Locate every blood parasite and identify its species.
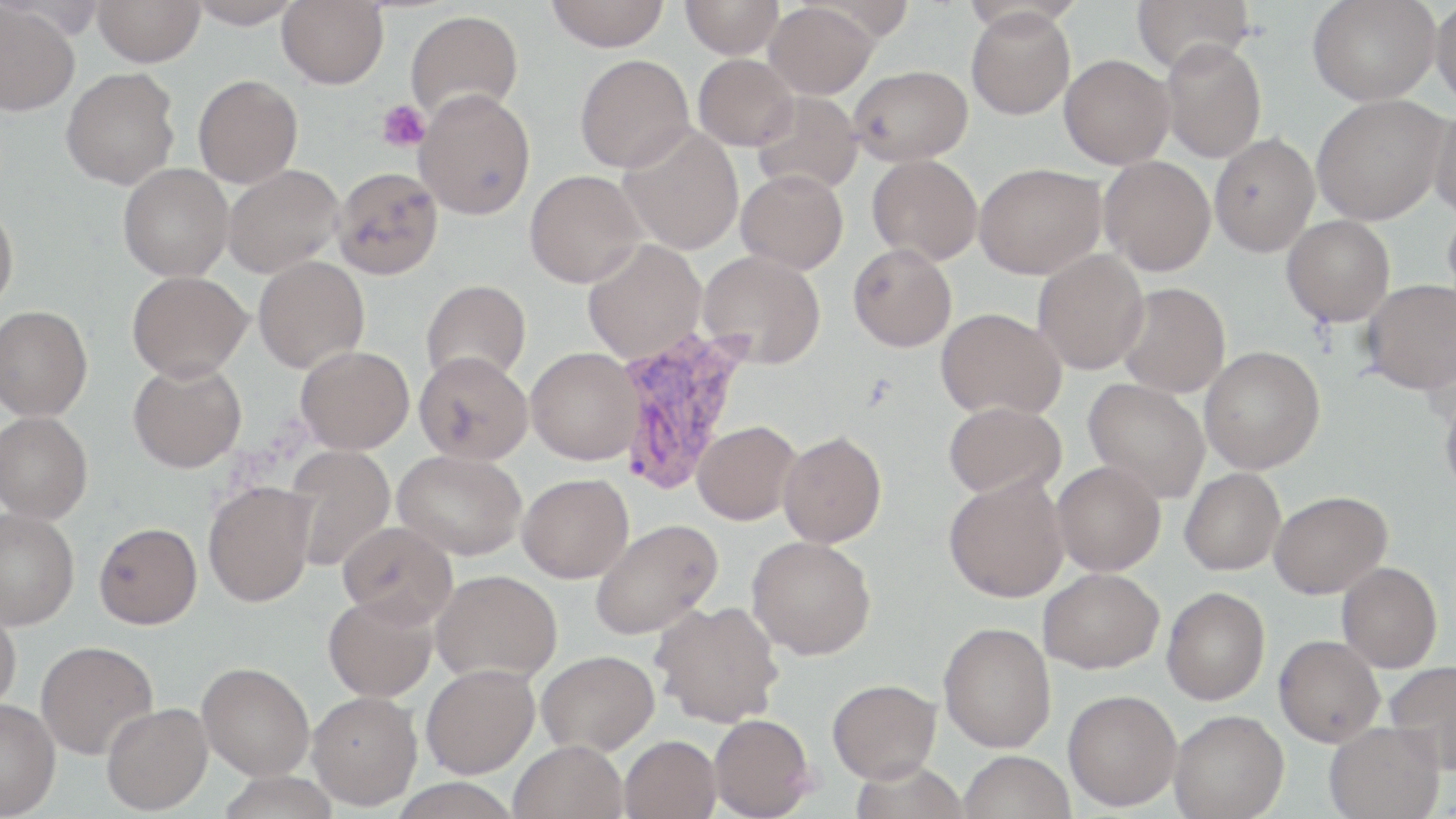

Approximate bounding boxes as (x1, y1, x2, y2) in pixels.
Plasmodium vivax-infected red blood cells: (615, 328, 750, 496).
No Plasmodium falciparum, Plasmodium ovale, Plasmodium malariae, Babesia divergens, or Trypanosoma brucei observed.

Summary:
  - Uninfected red blood cell locations: (93, 0, 205, 66), (185, 0, 305, 28), (546, 0, 670, 51), (681, 0, 783, 59), (1132, 0, 1256, 72), (1308, 0, 1440, 106), (277, 1, 388, 89), (1431, 1, 1456, 110), (0, 3, 80, 115), (764, 3, 878, 98), (966, 7, 1076, 120), (405, 10, 524, 123), (1159, 38, 1267, 163), (575, 54, 694, 173), (693, 54, 798, 150), (1059, 54, 1175, 169), (848, 65, 972, 166), (61, 68, 180, 190), (193, 75, 303, 188), (415, 88, 535, 220), (751, 92, 863, 195), (1311, 95, 1448, 225), (1429, 103, 1456, 221), (618, 127, 744, 255), (1209, 133, 1320, 257), (867, 154, 982, 265), (1099, 156, 1216, 276), (118, 163, 234, 281), (974, 163, 1106, 279), (222, 164, 344, 277), (332, 167, 444, 280), (524, 170, 646, 288), (736, 170, 848, 274), (1443, 200, 1456, 312), (0, 203, 18, 312), (1282, 215, 1395, 326), (583, 241, 706, 363), (848, 243, 957, 352), (698, 250, 826, 368), (1032, 250, 1149, 375), (253, 256, 369, 373), (127, 270, 251, 381), (421, 279, 531, 386), (1361, 279, 1456, 394), (1117, 283, 1230, 398), (0, 306, 93, 422), (936, 307, 1066, 419), (296, 345, 414, 454), (1199, 346, 1325, 474), (525, 347, 644, 464), (413, 350, 533, 465), (128, 360, 246, 473), (1084, 379, 1210, 503), (1440, 388, 1456, 501), (943, 400, 1066, 499), (0, 411, 93, 523), (692, 420, 800, 524), (778, 431, 887, 547), (287, 444, 395, 571), (393, 449, 527, 560), (1052, 461, 1165, 576), (1180, 468, 1285, 575), (517, 473, 634, 583), (944, 474, 1069, 602), (202, 480, 316, 607), (1268, 490, 1392, 598), (1, 507, 79, 630), (589, 519, 722, 640), (337, 521, 458, 627), (94, 522, 202, 629), (746, 535, 876, 659), (1336, 562, 1442, 673), (1038, 568, 1164, 674), (431, 570, 563, 684), (1162, 586, 1269, 705), (323, 593, 438, 702), (650, 599, 783, 727), (0, 605, 21, 714), (938, 621, 1056, 752), (1273, 635, 1384, 747), (36, 640, 158, 759), (536, 649, 659, 755), (1384, 660, 1456, 774), (197, 661, 315, 780), (421, 663, 539, 778), (827, 678, 941, 783), (1062, 689, 1182, 811), (307, 690, 422, 810), (0, 698, 60, 818), (101, 702, 213, 815), (1169, 709, 1289, 819), (709, 713, 814, 818), (1324, 721, 1445, 819), (620, 735, 721, 819), (509, 739, 629, 819), (957, 750, 1076, 819)
  - Platelet locations: (377, 100, 430, 152)
  - Slide-level diagnosis: Plasmodium vivax
  - Magnification: 1000x
  - Image size: 1456×819 pixels
  - Stain: May-Grünwald-Giemsa
  - Modality: optical microscopy
  - Preparation: thin blood film
  - Field of view: single